Point out malaria parasites and leukocytes.
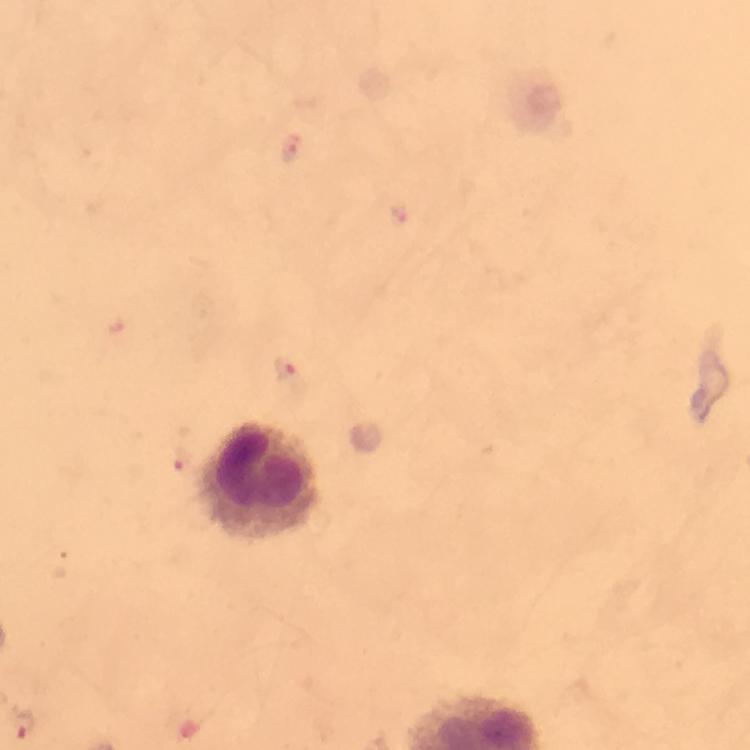

Approximate centers as (x, y) in pixels.
Malaria parasites: (291, 149), (286, 375), (180, 461), (22, 725).
Leukocytes: (260, 483).

Smartphone photograph taken through a microscope. A crop from one field of view. 100x magnification. Image is 750×750 pixels. From a diagnostic examination for malaria. Immersion oil was used. Giemsa stain. Thick smear.